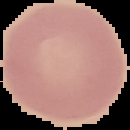

From a thin blood smear. Malaria status: uninfected. Image is 130×130 pixels. Cell region segmented out of the field of view; the surrounding area is masked to black.